Locate and identify every blood parasite.
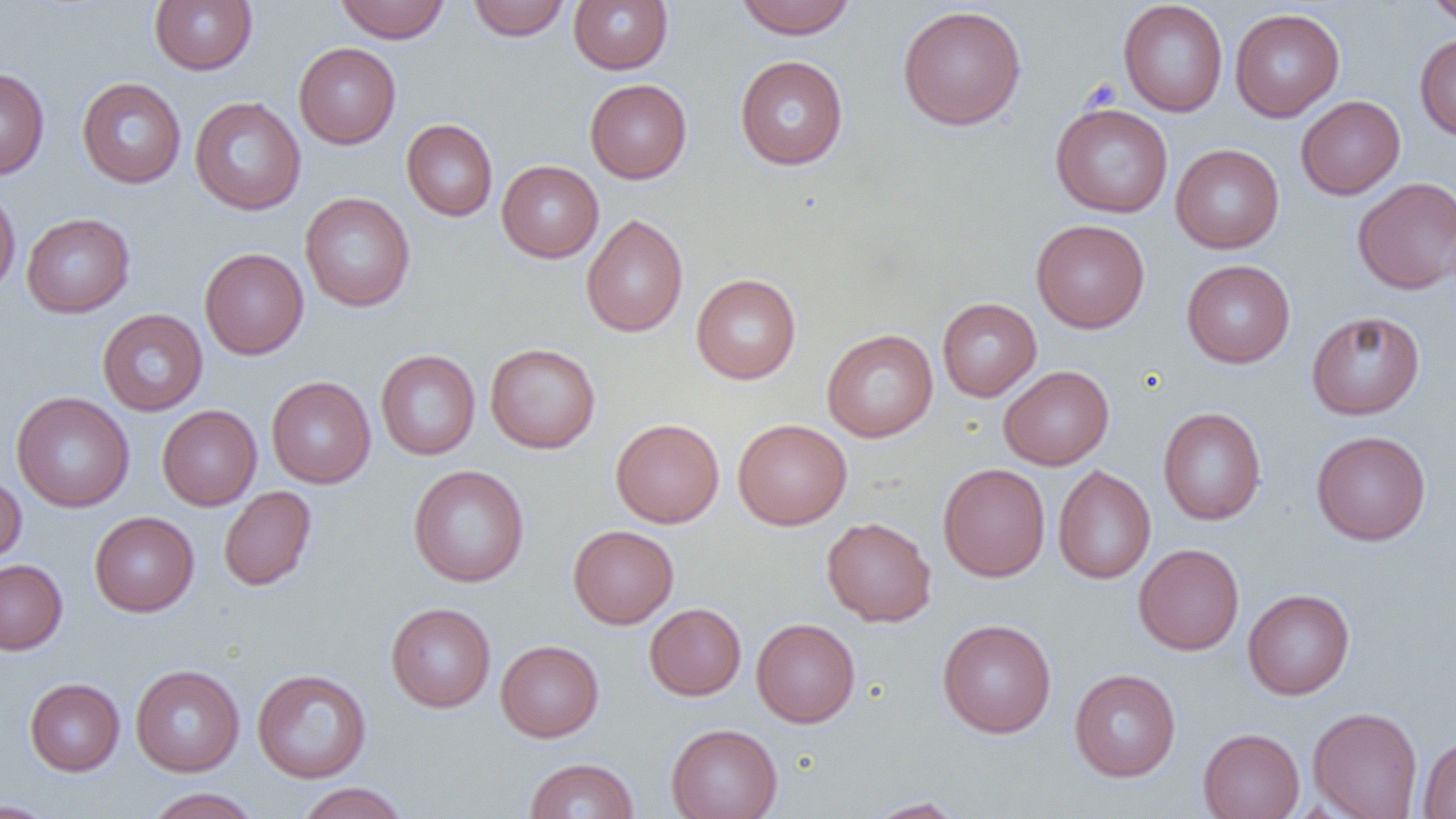
No blood parasites seen.

slide-level diagnosis = negative for blood parasites
image size = 1456×819 pixels
field of view = single
magnification = 1000x
modality = light microscopy
uninfected red blood cell locations = approximate bounding boxes as named x1/y1/x2/y2 corners in pixels: (x1=149, y1=0, x2=257, y2=75), (x1=335, y1=0, x2=451, y2=43), (x1=467, y1=0, x2=570, y2=41), (x1=735, y1=0, x2=856, y2=39), (x1=1423, y1=0, x2=1456, y2=26), (x1=569, y1=1, x2=673, y2=74), (x1=1118, y1=1, x2=1228, y2=117), (x1=897, y1=4, x2=1027, y2=131), (x1=1230, y1=8, x2=1345, y2=121), (x1=1414, y1=33, x2=1456, y2=141), (x1=293, y1=42, x2=401, y2=149), (x1=735, y1=55, x2=848, y2=170), (x1=0, y1=67, x2=50, y2=180), (x1=77, y1=77, x2=186, y2=189), (x1=585, y1=78, x2=692, y2=184), (x1=75, y1=85, x2=300, y2=194), (x1=1296, y1=95, x2=1405, y2=199), (x1=189, y1=96, x2=306, y2=215), (x1=1050, y1=102, x2=1173, y2=218), (x1=401, y1=119, x2=498, y2=221), (x1=1170, y1=144, x2=1284, y2=253), (x1=496, y1=160, x2=603, y2=263), (x1=1353, y1=176, x2=1456, y2=295), (x1=0, y1=185, x2=21, y2=296), (x1=300, y1=192, x2=415, y2=312), (x1=21, y1=213, x2=135, y2=318), (x1=581, y1=213, x2=688, y2=337), (x1=1031, y1=219, x2=1149, y2=333), (x1=199, y1=247, x2=309, y2=360), (x1=1182, y1=259, x2=1295, y2=368), (x1=691, y1=273, x2=801, y2=384), (x1=937, y1=297, x2=1042, y2=401), (x1=97, y1=309, x2=208, y2=415), (x1=1306, y1=311, x2=1425, y2=420), (x1=822, y1=329, x2=938, y2=443), (x1=485, y1=343, x2=601, y2=453), (x1=375, y1=349, x2=481, y2=460), (x1=999, y1=365, x2=1114, y2=470), (x1=266, y1=376, x2=376, y2=488), (x1=11, y1=392, x2=134, y2=513), (x1=157, y1=404, x2=262, y2=510), (x1=1157, y1=407, x2=1266, y2=525), (x1=610, y1=418, x2=725, y2=528), (x1=732, y1=419, x2=852, y2=530), (x1=1311, y1=430, x2=1431, y2=546), (x1=937, y1=463, x2=1050, y2=582), (x1=408, y1=465, x2=529, y2=587), (x1=1053, y1=465, x2=1155, y2=584), (x1=0, y1=473, x2=26, y2=565), (x1=219, y1=486, x2=317, y2=591), (x1=89, y1=511, x2=199, y2=617), (x1=821, y1=517, x2=936, y2=627), (x1=568, y1=525, x2=679, y2=629), (x1=1133, y1=543, x2=1244, y2=655), (x1=0, y1=559, x2=67, y2=654), (x1=1242, y1=588, x2=1355, y2=700), (x1=385, y1=602, x2=496, y2=712), (x1=644, y1=603, x2=746, y2=700), (x1=751, y1=618, x2=860, y2=727), (x1=938, y1=618, x2=1057, y2=738), (x1=495, y1=639, x2=604, y2=742), (x1=130, y1=664, x2=244, y2=776), (x1=251, y1=668, x2=372, y2=783), (x1=1069, y1=668, x2=1181, y2=781), (x1=24, y1=677, x2=125, y2=776), (x1=1308, y1=706, x2=1422, y2=819), (x1=666, y1=723, x2=782, y2=819), (x1=1198, y1=728, x2=1304, y2=819), (x1=1418, y1=733, x2=1456, y2=819), (x1=524, y1=758, x2=639, y2=818), (x1=295, y1=782, x2=410, y2=819), (x1=144, y1=787, x2=260, y2=819), (x1=864, y1=796, x2=967, y2=818), (x1=0, y1=799, x2=61, y2=819)
preparation = thin blood film